Assess the morphology of the erythrocytes.
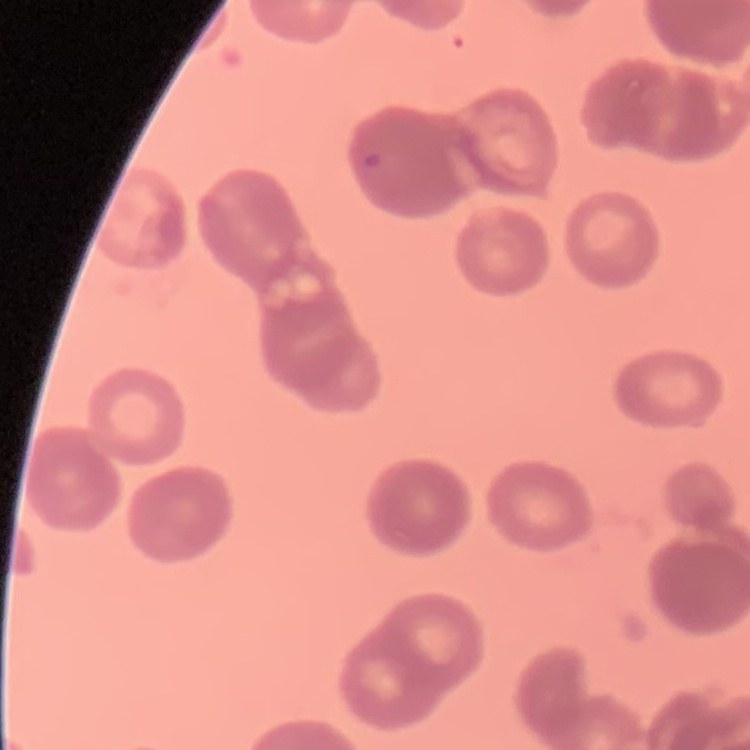

Rouleaux formation.

Square crop of a larger photomicrograph. Thin blood smear. Field's or Giemsa stain.